Describe the morphology of the erythrocytes.
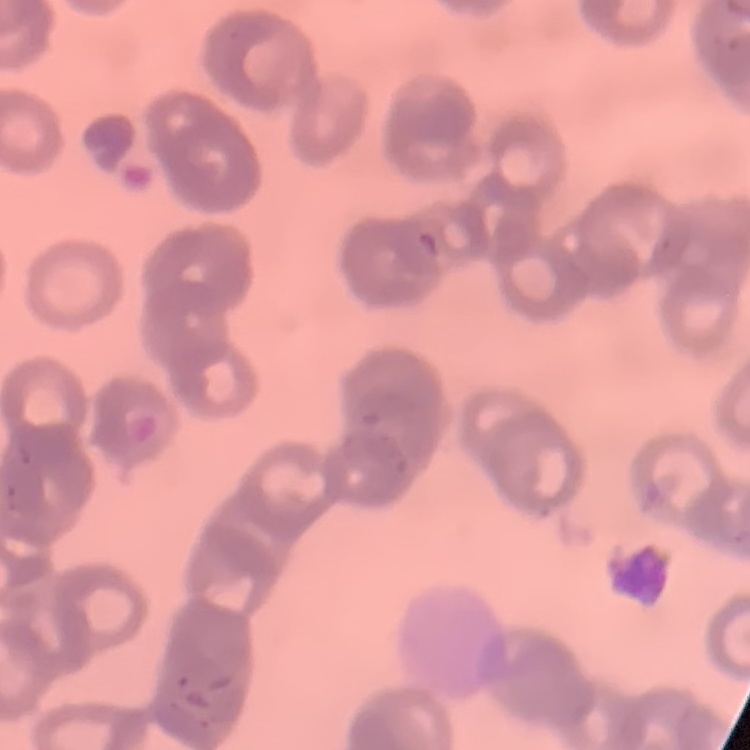

Rouleaux formation.

Thin blood smear. Field's or Giemsa stain. One tile cut from a larger photomicrograph.